Classify this cell by malaria status.
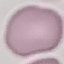
It is uninfected.

image type = automatically extracted cell patch, resized to 64 × 64 pixels
capture = smartphone camera at the microscope eyepiece
preparation = thin blood film
stain = Giemsa